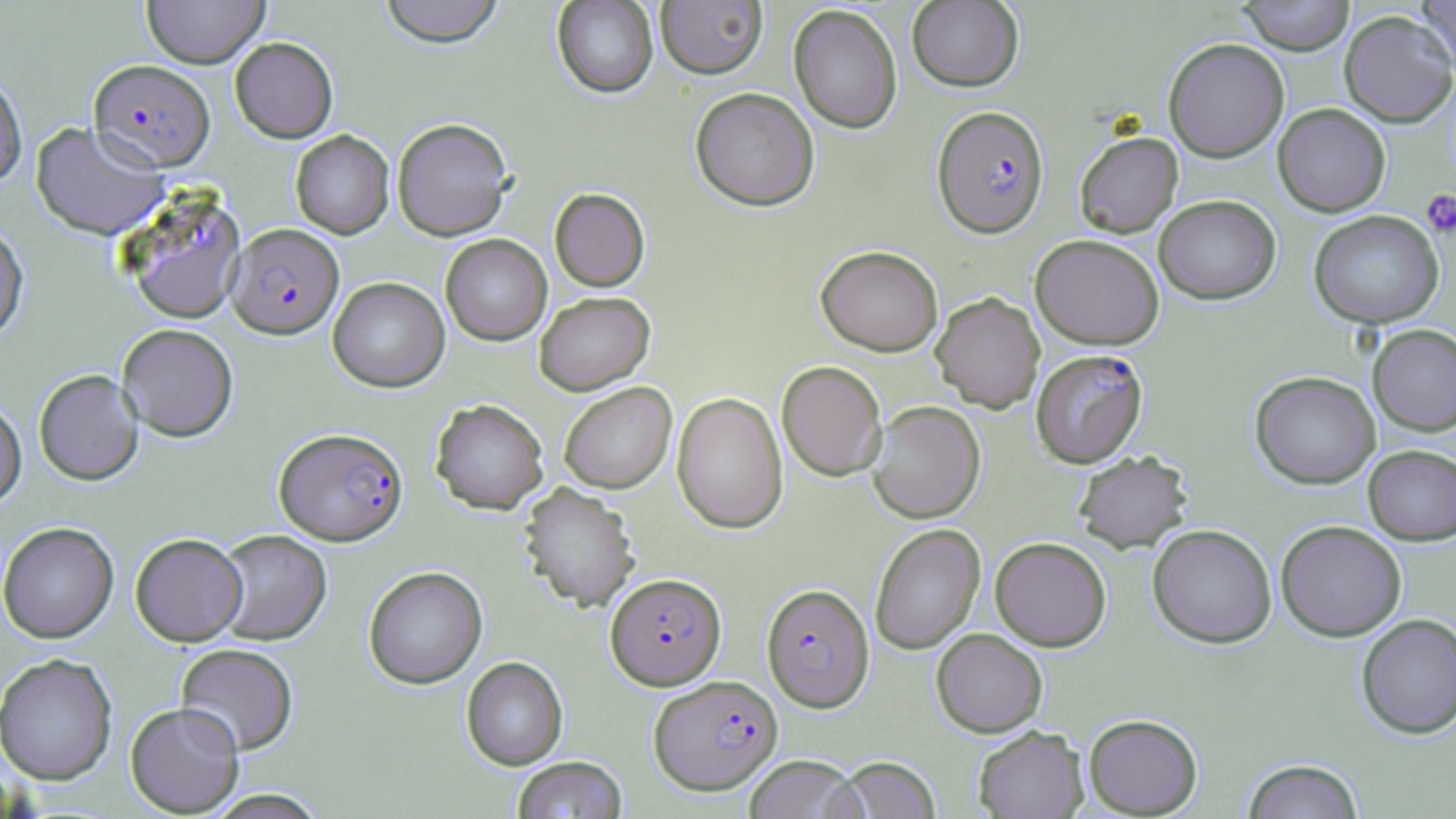 Approximate bounding boxes as (x1,y1)-(x2,y2) corner pairs in pixels. Uninfected red blood cell locations: (142,0)-(270,67), (378,0)-(506,48), (907,0)-(1024,92), (1239,0)-(1355,55), (1416,0)-(1456,75), (552,1)-(659,98), (656,1)-(768,78), (789,4)-(903,134), (1339,10)-(1456,127), (230,37)-(338,143), (1163,38)-(1289,162), (0,72)-(27,188), (690,87)-(820,211), (1273,103)-(1391,217), (392,117)-(513,240), (31,121)-(168,240), (291,130)-(394,238), (1074,131)-(1183,237), (550,187)-(650,291), (1154,194)-(1281,304), (1309,210)-(1444,328), (0,222)-(29,342), (441,234)-(552,345), (1030,234)-(1165,350), (816,244)-(944,356), (328,277)-(449,392), (534,291)-(655,395), (931,292)-(1045,412), (117,323)-(239,441), (1368,324)-(1456,436), (777,361)-(887,481), (34,369)-(144,485), (1250,371)-(1381,489), (559,382)-(676,493), (672,392)-(788,533), (430,398)-(548,514), (0,400)-(26,508), (867,401)-(985,523), (1363,445)-(1456,545), (1073,449)-(1193,553), (519,483)-(639,613), (1276,520)-(1407,641), (0,522)-(118,643), (869,524)-(985,655), (1147,524)-(1277,648), (214,529)-(332,645), (130,533)-(247,646), (990,536)-(1111,651), (363,566)-(487,689), (1356,613)-(1456,739), (931,628)-(1048,737), (175,643)-(299,755), (0,653)-(118,784), (461,656)-(568,770), (125,701)-(245,816), (1084,713)-(1203,817), (973,725)-(1089,818), (743,755)-(866,819), (511,756)-(628,818), (838,757)-(942,818), (1242,758)-(1364,819), (200,789)-(332,818). Plasmodium falciparum-infected red blood cell locations: (89,59)-(215,171), (932,105)-(1049,237), (122,190)-(248,324), (227,223)-(343,339), (1031,349)-(1148,468), (275,427)-(408,545), (606,573)-(726,690), (762,583)-(874,711), (649,675)-(783,795). Platelet locations: (1422,189)-(1456,237). Slide-level diagnosis: Plasmodium falciparum. Light microscopy. May-Grünwald-Giemsa stain. Captured at 1000x magnification. One field of a larger specimen. Image is 1456×819 pixels. Thin blood smear.